Locate every blood parasite and identify its species.
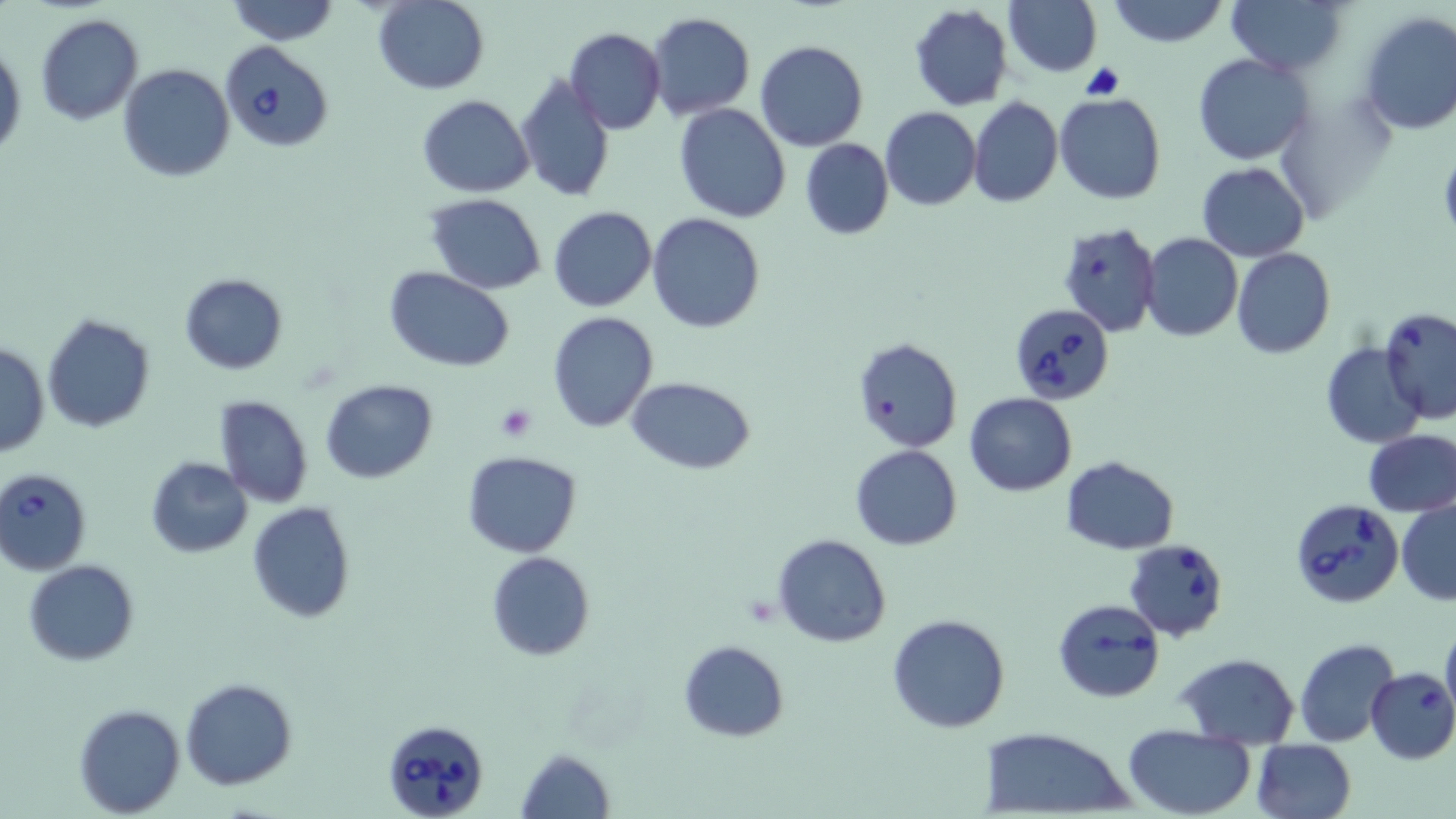

Approximate bounding boxes as named x1/y1/x2/y2 corners in pixels.
Babesia divergens-infected red blood cells: (x1=220, y1=40, x2=334, y2=154), (x1=1013, y1=307, x2=1116, y2=405), (x1=0, y1=468, x2=93, y2=573), (x1=1290, y1=500, x2=1404, y2=609), (x1=1125, y1=538, x2=1228, y2=639), (x1=1052, y1=598, x2=1166, y2=703), (x1=381, y1=718, x2=490, y2=819).
No Plasmodium falciparum, Plasmodium ovale, Plasmodium malariae, Plasmodium vivax, or Trypanosoma brucei observed.

Summary:
  - Uninfected red blood cell locations: (x1=1003, y1=0, x2=1100, y2=78), (x1=1108, y1=0, x2=1228, y2=46), (x1=1227, y1=0, x2=1347, y2=77), (x1=226, y1=1, x2=342, y2=46), (x1=373, y1=1, x2=489, y2=94), (x1=908, y1=5, x2=1013, y2=111), (x1=1356, y1=11, x2=1456, y2=134), (x1=647, y1=13, x2=754, y2=120), (x1=33, y1=15, x2=143, y2=125), (x1=564, y1=27, x2=666, y2=134), (x1=0, y1=38, x2=24, y2=161), (x1=755, y1=40, x2=868, y2=151), (x1=1195, y1=53, x2=1312, y2=164), (x1=119, y1=64, x2=235, y2=183), (x1=515, y1=74, x2=616, y2=203), (x1=1055, y1=93, x2=1168, y2=205), (x1=417, y1=95, x2=533, y2=197), (x1=969, y1=97, x2=1062, y2=208), (x1=674, y1=103, x2=791, y2=221), (x1=879, y1=107, x2=981, y2=211), (x1=799, y1=138, x2=893, y2=240), (x1=1196, y1=162, x2=1309, y2=262), (x1=426, y1=195, x2=547, y2=293), (x1=549, y1=205, x2=658, y2=313), (x1=648, y1=214, x2=765, y2=332), (x1=1058, y1=220, x2=1161, y2=337), (x1=1140, y1=234, x2=1242, y2=342), (x1=1232, y1=249, x2=1334, y2=360), (x1=386, y1=268, x2=514, y2=370), (x1=179, y1=273, x2=288, y2=375), (x1=1380, y1=306, x2=1456, y2=425), (x1=547, y1=311, x2=659, y2=433), (x1=42, y1=314, x2=155, y2=434), (x1=851, y1=337, x2=963, y2=454), (x1=1322, y1=342, x2=1427, y2=448), (x1=1, y1=343, x2=48, y2=457), (x1=625, y1=375, x2=757, y2=473), (x1=320, y1=379, x2=437, y2=484), (x1=964, y1=392, x2=1077, y2=496), (x1=213, y1=395, x2=314, y2=508), (x1=1363, y1=428, x2=1456, y2=518), (x1=850, y1=446, x2=963, y2=550), (x1=462, y1=451, x2=584, y2=558), (x1=145, y1=456, x2=254, y2=558), (x1=1063, y1=456, x2=1179, y2=554), (x1=1397, y1=499, x2=1456, y2=604), (x1=247, y1=501, x2=356, y2=623), (x1=773, y1=533, x2=891, y2=647), (x1=485, y1=552, x2=597, y2=661), (x1=25, y1=560, x2=139, y2=665), (x1=886, y1=613, x2=1012, y2=733), (x1=1440, y1=620, x2=1456, y2=728), (x1=1295, y1=638, x2=1400, y2=748), (x1=679, y1=640, x2=790, y2=742), (x1=1176, y1=653, x2=1299, y2=747), (x1=1365, y1=667, x2=1456, y2=764), (x1=180, y1=677, x2=300, y2=790), (x1=74, y1=704, x2=187, y2=817), (x1=1122, y1=725, x2=1255, y2=816), (x1=976, y1=726, x2=1136, y2=817), (x1=1251, y1=739, x2=1357, y2=819), (x1=515, y1=746, x2=616, y2=819)
  - Platelet locations: (x1=495, y1=405, x2=536, y2=443)
  - Slide-level diagnosis: Babesia divergens
  - Stain: May-Grünwald-Giemsa
  - Modality: light microscopy
  - Preparation: thin blood film
  - Magnification: 1000x
  - Image size: 1456×819 pixels
  - Field of view: single